Classify this cell by malaria status.
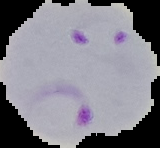
It is parasitized.

preparation = thin blood smear
image type = cell region segmented out of the field of view; surrounding area masked to black
image size = 160×148 pixels